Assess this cell for malaria.
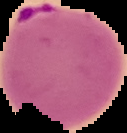
Parasitized.

Cell region segmented out of the field of view; the surrounding area is masked to black. From a thin blood smear. Image is 127×133 pixels.